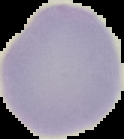 Result: negative for Plasmodium parasites. Cell region segmented out of the field of view; the surrounding area is masked to black. Image is 124×139 pixels. From a thin blood smear.